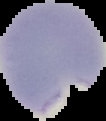

Malaria status: parasitized. Image is 106×121 pixels. From a thin blood smear. Cell region segmented out of the field of view; the surrounding area is masked to black.